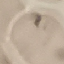 Result: no malaria parasites detected. Giemsa-stained preparation. Cell patch, automatically extracted from a larger field of view and resized to 64 × 64 pixels. Thin blood film. Photographed with a smartphone camera at the microscope eyepiece.